Mark where platelets are.
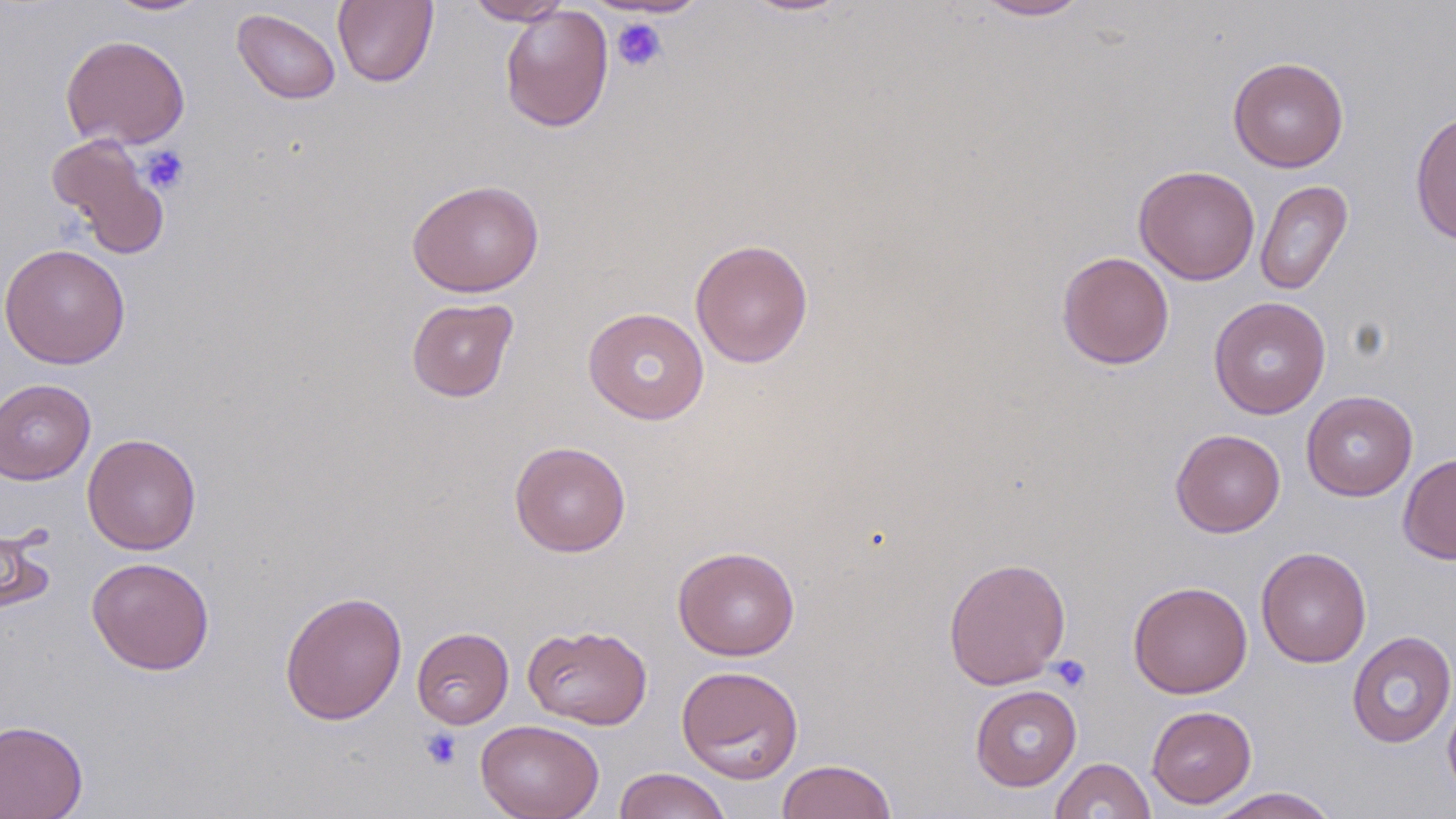
Approximate bounding boxes as (x1, y1, x2, y2) in pixels.
Platelets: (611, 18, 667, 72), (140, 146, 190, 195), (1049, 655, 1091, 692), (420, 727, 463, 770).

Summary:
  - Uninfected red blood cell locations: (100, 0, 214, 16), (332, 0, 439, 88), (465, 0, 572, 25), (739, 0, 852, 17), (972, 0, 1092, 21), (499, 5, 614, 133), (231, 8, 341, 104), (60, 34, 190, 150), (1227, 56, 1349, 172), (1409, 110, 1456, 246), (47, 134, 169, 258), (1133, 165, 1260, 285), (406, 179, 544, 297), (1255, 179, 1353, 295), (690, 239, 814, 368), (0, 243, 131, 369), (1056, 251, 1175, 370), (406, 297, 519, 402), (1208, 297, 1331, 419), (583, 307, 709, 425), (0, 378, 96, 485), (1301, 390, 1418, 501), (1170, 428, 1285, 537), (82, 433, 202, 554), (510, 441, 631, 557), (1398, 453, 1456, 564), (0, 523, 55, 617), (672, 545, 800, 661), (1256, 546, 1372, 668), (87, 556, 215, 675), (943, 556, 1071, 690), (1128, 580, 1253, 699), (279, 590, 407, 725), (523, 624, 652, 730), (411, 627, 514, 729), (1346, 631, 1456, 749), (676, 665, 804, 783), (970, 684, 1082, 790), (1443, 687, 1456, 808), (1146, 705, 1257, 808), (476, 719, 604, 819), (0, 720, 88, 819), (1050, 757, 1156, 818), (776, 759, 898, 819), (613, 767, 732, 819), (1206, 787, 1341, 818)
  - Slide-level diagnosis: no evidence of blood parasites
  - Image size: 1456×819 pixels
  - Stain: May-Grünwald-Giemsa
  - Field of view: single
  - Modality: light microscopy
  - Preparation: thin blood smear
  - Magnification: 1000x